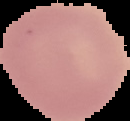

Summary:
  - Image type: segmented cell region on a black background
  - Image size: 130×121 pixels
  - Preparation: thin blood film
  - Malaria status: uninfected